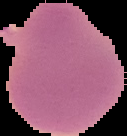 Segmented cell region on a black background. From a thin blood smear. Malaria status: uninfected. Image is 127×136 pixels.